Identify the parasite.
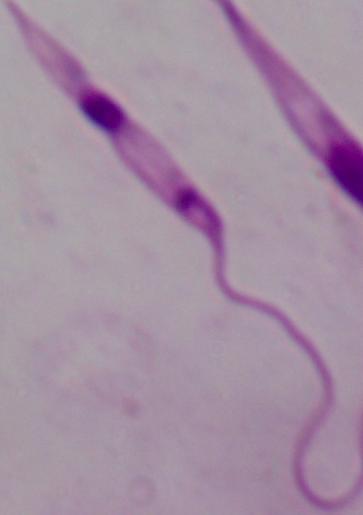

Leishmania.

Photomicrograph. 1000x magnification.